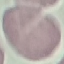

Summary:
  - Result: no malaria parasites detected
  - Capture: smartphone camera at the microscope eyepiece
  - Stain: Giemsa
  - Preparation: thin blood smear
  - Image type: cell patch, automatically extracted from a larger field of view and resized to 64 × 64 pixels